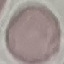
malaria status = uninfected
capture = smartphone camera at the microscope eyepiece
stain = Giemsa
image type = automatically extracted cell patch, resized to 64 × 64 pixels
preparation = thin smear